Assess this cell for malaria.
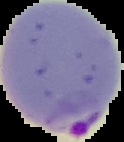

It is parasitized.

Image is 124×142 pixels. From a thin blood smear. Segmented cell region on a black background.